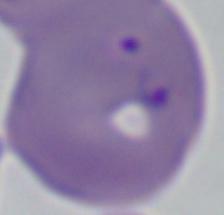

identification = Babesia
magnification = 1000x
modality = micrograph